Locate every leukocyte (white blood cell).
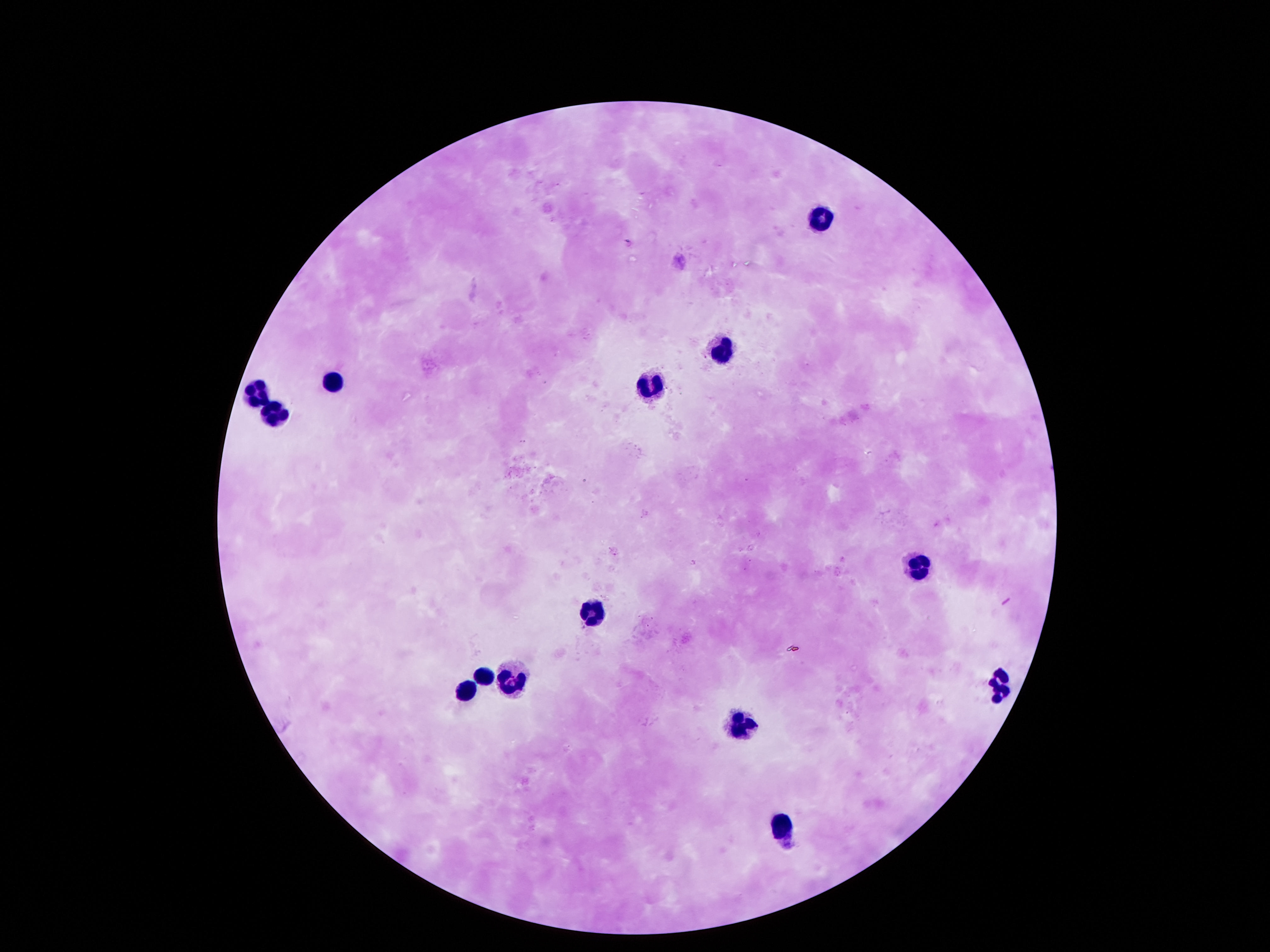
Approximate object centers, in pixels from the top-left corner.
Leukocytes: (x=823, y=215), (x=719, y=352), (x=332, y=378), (x=648, y=384), (x=257, y=394), (x=277, y=410), (x=920, y=568), (x=590, y=612), (x=480, y=674), (x=509, y=680), (x=1000, y=680), (x=467, y=684), (x=742, y=720), (x=781, y=832).

Single field of view. Giemsa-stained preparation. Image is 1270×952 pixels. 100x magnification. Smartphone photograph taken through the microscope eyepiece. Thick blood smear. Patient malaria status: uninfected.